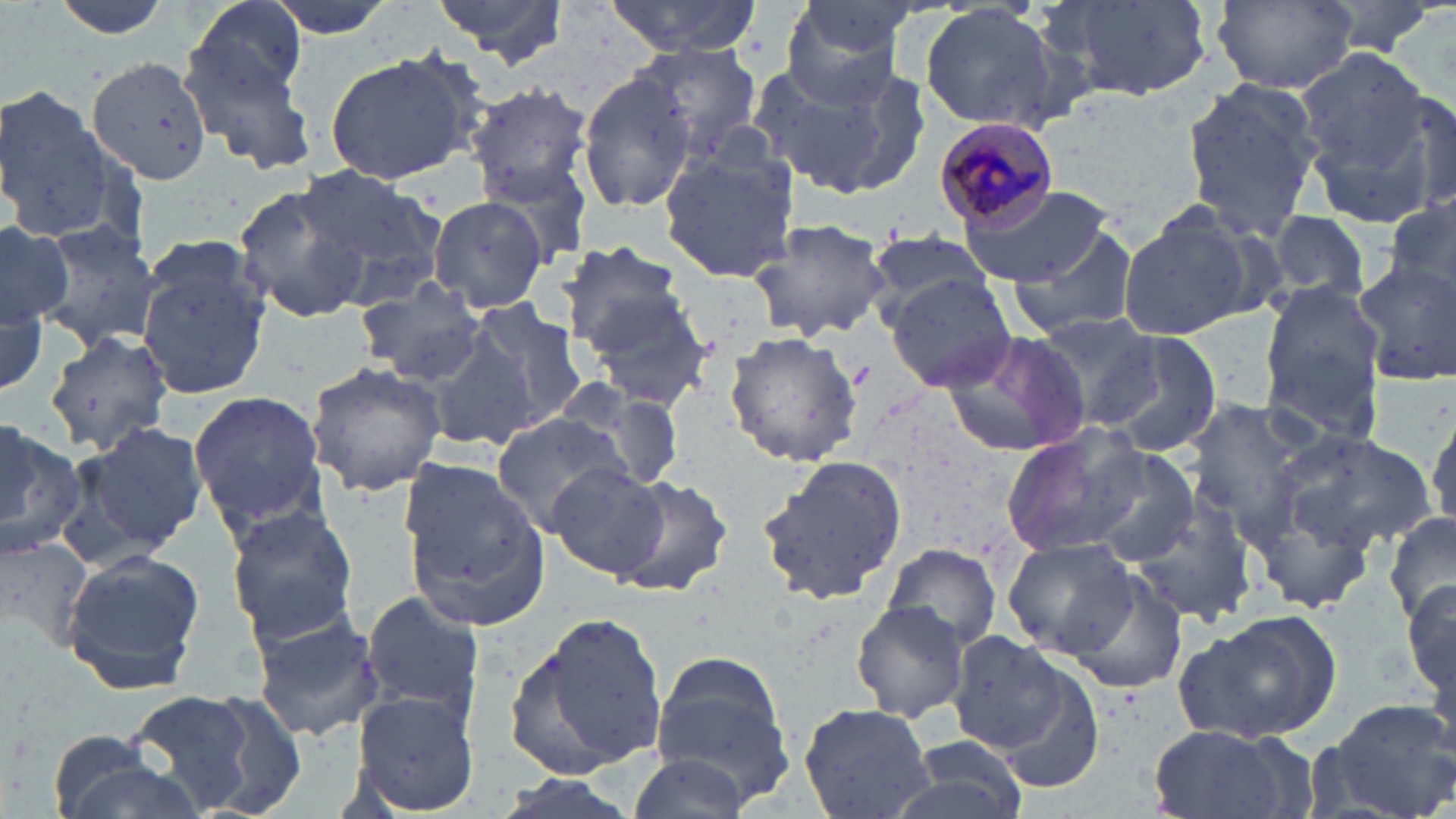
slide-level diagnosis = Plasmodium malariae
uninfected red blood cell locations = approximate bounding boxes as (x1,y1)-(x2,y2) corner pairs in pixels: (43,0)-(181,41), (187,0)-(311,101), (255,0)-(404,40), (434,0)-(570,67), (603,0)-(763,58), (779,0)-(918,106), (1048,0)-(1218,101), (1211,0)-(1360,92), (1309,0)-(1445,59), (920,4)-(1066,134), (179,33)-(320,173), (626,40)-(763,154), (1293,46)-(1433,173), (321,48)-(488,185), (746,52)-(930,200), (88,58)-(214,186), (578,72)-(699,213), (1177,74)-(1323,238), (0,83)-(119,242), (466,83)-(594,202), (1305,91)-(1448,226), (658,150)-(801,284), (283,160)-(448,310), (960,182)-(1118,289), (232,183)-(378,323), (427,196)-(551,314), (1385,198)-(1456,304), (1115,202)-(1267,342), (1267,211)-(1374,308), (0,217)-(82,341), (744,217)-(893,342), (32,219)-(162,356), (1007,221)-(1143,342), (864,232)-(999,320), (555,240)-(690,356), (1351,252)-(1456,389), (136,253)-(270,400), (0,268)-(52,402), (883,273)-(1017,393), (354,277)-(488,388), (1260,282)-(1387,417), (582,287)-(720,409), (459,298)-(588,429), (1033,311)-(1168,427), (422,320)-(545,449), (43,330)-(175,458), (937,330)-(1092,461), (722,331)-(865,468), (1108,334)-(1223,462), (305,360)-(447,498), (550,378)-(689,495), (189,387)-(328,535), (1184,400)-(1324,540), (1426,403)-(1456,535), (489,412)-(634,536), (0,419)-(85,561), (60,419)-(207,563), (999,425)-(1150,559), (1273,430)-(1434,557), (1078,450)-(1204,567), (755,456)-(909,605), (398,458)-(553,632), (548,461)-(670,582), (606,470)-(734,600), (1124,493)-(1256,627), (224,503)-(361,646), (1385,510)-(1456,628), (1001,537)-(1140,658), (883,546)-(1003,647), (62,550)-(205,692), (1064,570)-(1191,697), (1402,574)-(1456,715), (358,587)-(486,728), (850,601)-(972,725), (248,605)-(382,744), (508,608)-(668,778), (1188,611)-(1346,742), (947,631)-(1068,754), (650,649)-(798,807), (995,662)-(1109,791), (123,687)-(265,817), (351,688)-(480,816), (194,689)-(310,815), (1314,697)-(1455,819), (797,702)-(938,819), (1144,724)-(1309,819), (892,732)-(1030,819), (39,736)-(188,819), (624,753)-(751,819)
modality = optical microscopy
field of view = one of a larger specimen
magnification = 1000x
preparation = thin blood film
stain = May-Grünwald-Giemsa
image size = 1456×819 pixels
Plasmodium malariae-infected red blood cell locations = approximate bounding boxes as (x1,y1)-(x2,y2) corner pairs in pixels: (933,116)-(1061,229)